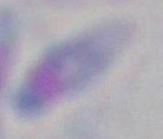
identification = Toxoplasma gondii
magnification = 1000x
modality = photomicrograph